Name the blood parasite species.
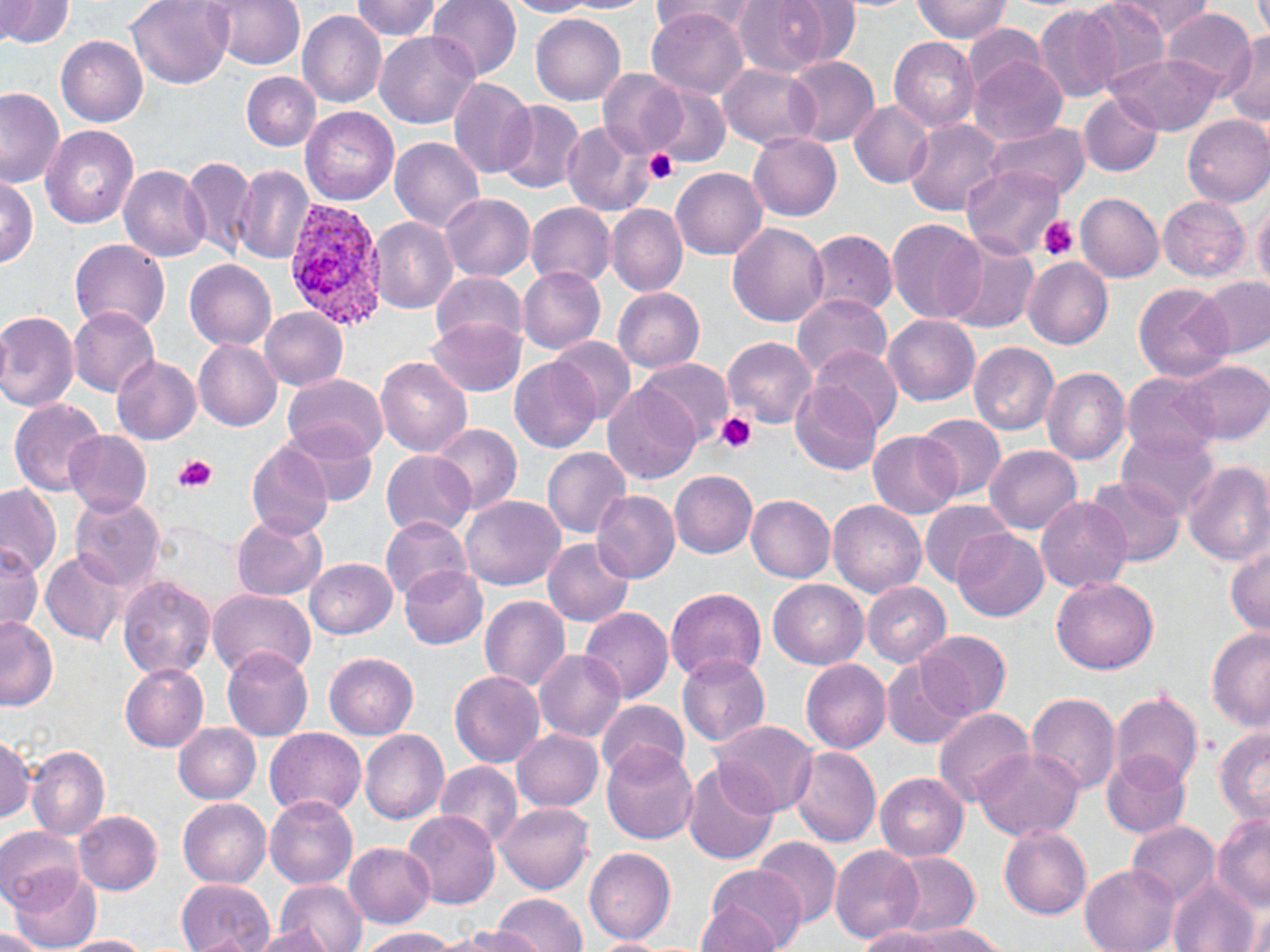

Plasmodium vivax.

magnification = 1000x
stain = May-Grünwald-Giemsa
field of view = one of a larger specimen
image size = 1270×952 pixels
preparation = thin blood smear
Plasmodium vivax-infected red blood cell locations = approximate bounding boxes as (x1, y1, x2, y2) in pixels: (281, 198, 392, 331)
modality = optical microscopy
platelet locations = approximate bounding boxes as (x1, y1, x2, y2) in pixels: (645, 149, 678, 185), (1040, 216, 1078, 261), (715, 412, 757, 455), (173, 454, 215, 490)
uninfected red blood cell locations = approximate bounding boxes as (x1, y1, x2, y2) in pixels: (1, 0, 74, 49), (126, 0, 233, 88), (352, 0, 442, 41), (427, 0, 521, 80), (503, 0, 595, 17), (561, 0, 656, 14), (650, 0, 757, 40), (773, 0, 863, 70), (912, 0, 1012, 43), (1078, 0, 1173, 90), (1112, 0, 1214, 40), (205, 1, 306, 71), (731, 1, 836, 78), (1034, 5, 1122, 103), (647, 8, 749, 99), (1160, 8, 1256, 96), (298, 10, 386, 108), (530, 13, 625, 105), (961, 24, 1048, 99), (375, 30, 481, 129), (1221, 33, 1270, 127), (57, 36, 147, 127), (889, 37, 979, 131), (784, 54, 879, 147), (1108, 54, 1221, 135), (395, 56, 514, 166), (969, 56, 1068, 146), (719, 63, 820, 149), (598, 70, 688, 158), (241, 72, 321, 151), (448, 76, 536, 178), (648, 86, 732, 168), (0, 87, 66, 188), (1077, 93, 1164, 177), (495, 100, 586, 195), (848, 101, 933, 188), (299, 106, 400, 204), (1182, 114, 1270, 207), (904, 118, 1007, 217), (560, 120, 655, 217), (986, 123, 1093, 200), (41, 126, 139, 230), (747, 132, 841, 221), (390, 137, 485, 231), (181, 157, 256, 259), (233, 164, 316, 264), (119, 165, 210, 261), (960, 165, 1064, 259), (671, 168, 767, 260), (1, 177, 38, 267), (1076, 192, 1164, 283), (440, 194, 535, 281), (1158, 196, 1250, 282), (1253, 200, 1270, 299), (525, 202, 616, 288), (606, 204, 687, 296), (369, 217, 458, 314), (886, 217, 987, 324), (727, 223, 830, 327), (807, 230, 898, 317), (943, 234, 1039, 335), (70, 239, 170, 334), (1022, 256, 1113, 350), (185, 260, 276, 350), (517, 266, 605, 354), (430, 272, 528, 351), (1197, 277, 1270, 358), (1133, 282, 1234, 381), (613, 287, 704, 372), (792, 292, 892, 380), (68, 307, 159, 397), (260, 308, 348, 390), (0, 310, 80, 412), (882, 314, 981, 406), (426, 318, 526, 396), (549, 336, 638, 425), (723, 337, 817, 428), (193, 339, 283, 430), (968, 342, 1059, 435), (806, 345, 902, 437), (110, 355, 202, 445), (376, 357, 472, 458), (634, 357, 734, 447), (510, 358, 603, 453), (1175, 360, 1270, 445), (1041, 369, 1130, 466), (283, 372, 389, 459), (1122, 372, 1220, 459), (602, 380, 703, 484), (791, 380, 882, 475), (9, 400, 106, 497), (915, 413, 1007, 501), (280, 422, 377, 506), (430, 423, 522, 517), (867, 429, 962, 519), (63, 430, 152, 516), (1117, 430, 1221, 518), (246, 442, 333, 541), (985, 445, 1081, 533), (542, 447, 630, 537), (382, 450, 475, 539), (1182, 460, 1270, 565), (669, 470, 758, 558), (1086, 475, 1186, 565), (0, 482, 60, 578), (590, 490, 681, 582), (746, 494, 835, 582), (70, 495, 166, 594), (461, 495, 566, 591), (1036, 496, 1132, 593), (919, 499, 1013, 585), (828, 500, 926, 598), (233, 514, 328, 602), (381, 516, 471, 602), (952, 528, 1048, 621), (543, 538, 635, 627), (1226, 544, 1270, 639), (0, 546, 43, 640), (41, 550, 130, 646), (305, 558, 398, 639), (400, 566, 487, 649), (117, 576, 215, 679), (1051, 576, 1159, 674), (769, 580, 869, 669), (862, 582, 952, 666), (665, 588, 766, 681), (208, 589, 317, 680), (480, 596, 571, 690), (580, 607, 674, 703), (0, 617, 58, 710), (1207, 627, 1270, 732), (915, 630, 1010, 720), (222, 648, 313, 741), (533, 649, 626, 741), (324, 652, 418, 739), (677, 654, 771, 747), (801, 659, 891, 753), (882, 660, 972, 749), (119, 663, 208, 752), (450, 671, 545, 768), (1025, 691, 1122, 794), (1109, 691, 1203, 792), (596, 700, 690, 783), (932, 708, 1035, 808), (708, 720, 820, 818), (174, 723, 261, 803), (1214, 726, 1270, 827), (263, 727, 366, 819), (512, 728, 604, 811), (360, 729, 449, 824), (1, 734, 35, 822), (0, 738, 72, 828), (601, 742, 697, 844), (26, 746, 109, 840), (788, 747, 881, 848), (973, 747, 1084, 841), (1101, 751, 1191, 839), (435, 761, 523, 849), (681, 762, 780, 865), (874, 772, 969, 861), (265, 796, 359, 889), (179, 798, 271, 887), (495, 802, 593, 894), (72, 811, 163, 895), (403, 811, 501, 911), (1211, 814, 1270, 911), (1125, 821, 1219, 907), (1000, 825, 1091, 919), (0, 826, 84, 911), (752, 836, 843, 928), (1196, 842, 1268, 952), (344, 843, 435, 927), (830, 845, 924, 943), (584, 847, 676, 944), (887, 851, 980, 936), (1079, 863, 1180, 952), (707, 866, 807, 952), (9, 867, 102, 951), (177, 878, 274, 952), (1167, 878, 1259, 951), (276, 879, 367, 952), (491, 894, 587, 952), (695, 904, 784, 951), (1241, 904, 1270, 950), (900, 924, 1008, 952), (249, 926, 340, 952), (444, 926, 540, 951), (854, 926, 963, 952), (357, 927, 457, 951), (1, 928, 50, 951), (60, 935, 149, 952), (582, 938, 679, 951)